Comment on the morphology of the erythrocytes.
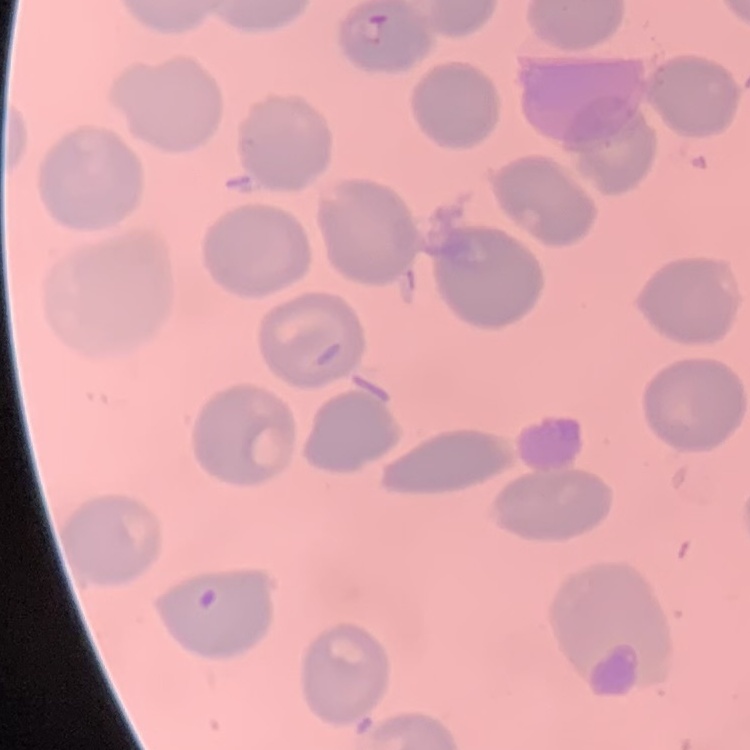

No rouleaux formation.

Summary:
  - Stain: Field's or Giemsa
  - Preparation: thin peripheral smear
  - Image type: one tile cut from a larger photomicrograph